Describe the morphology of the red blood cells.
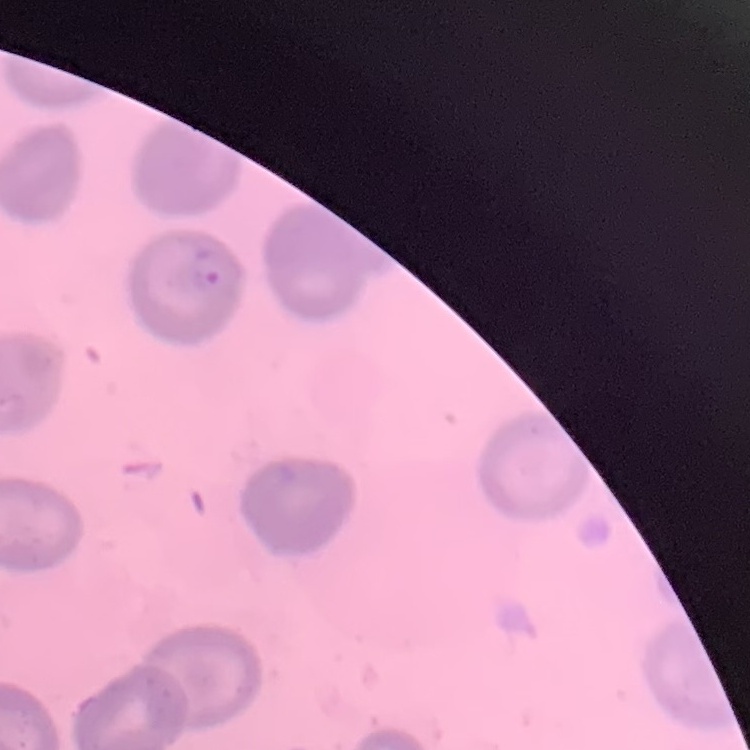
No rouleaux formation.

Stained with either Field's or Giemsa. Thin blood smear. Square crop of a larger photomicrograph.